Locate and identify every blood parasite.
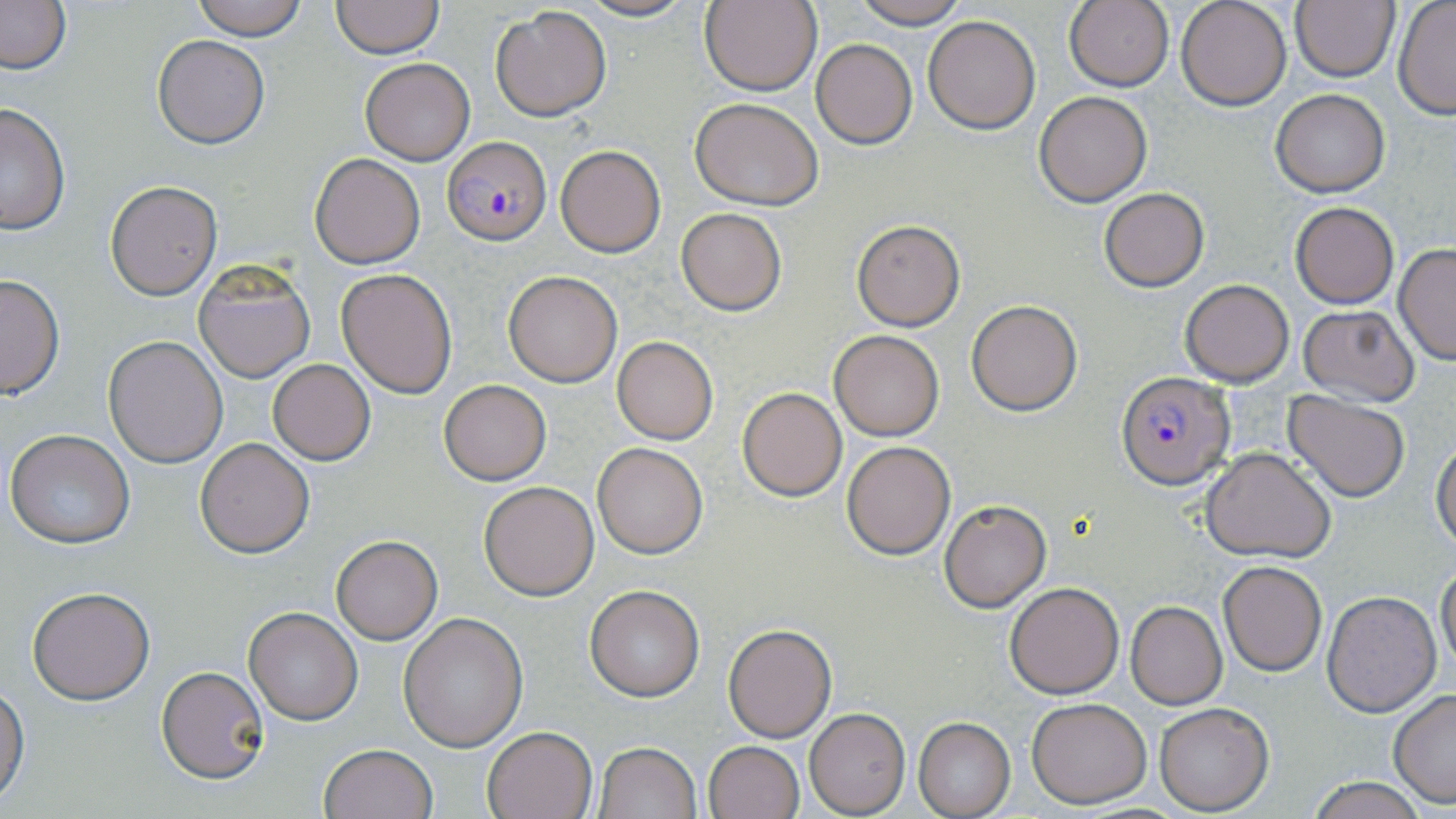
Approximate bounding boxes as (x1,y1)-(x2,y2) corner pairs in pixels.
Plasmodium falciparum-infected red blood cells: (443,135)-(551,245), (1115,371)-(1235,490).
No Plasmodium ovale, Plasmodium malariae, Plasmodium vivax, Babesia divergens, or Trypanosoma brucei observed.

Summary:
  - Uninfected red blood cell locations: (187,0)-(311,41), (575,0)-(696,21), (853,0)-(971,27), (1065,0)-(1176,92), (1176,0)-(1291,110), (1290,0)-(1398,83), (0,1)-(73,76), (330,1)-(444,59), (699,1)-(823,97), (1393,1)-(1456,120), (491,6)-(611,121), (922,16)-(1040,134), (152,34)-(271,149), (811,38)-(917,149), (359,58)-(474,165), (1270,90)-(1391,198), (1033,93)-(1152,207), (690,97)-(824,209), (0,103)-(71,234), (554,143)-(666,258), (311,153)-(424,268), (104,180)-(223,300), (1098,187)-(1210,292), (1289,202)-(1400,308), (677,208)-(786,315), (850,219)-(965,331), (1393,243)-(1456,365), (194,262)-(315,383), (335,267)-(457,398), (503,272)-(622,387), (0,273)-(65,398), (1179,279)-(1294,386), (967,301)-(1081,415), (1297,302)-(1420,405), (827,329)-(944,441), (103,335)-(229,468), (611,337)-(718,445), (268,359)-(376,466), (439,379)-(550,484), (738,387)-(848,501), (1285,393)-(1410,502), (5,429)-(135,549), (195,438)-(314,558), (1432,440)-(1456,553), (841,441)-(955,559), (592,442)-(709,558), (1201,447)-(1336,561), (479,481)-(600,600), (940,499)-(1051,611), (332,537)-(443,644), (1217,561)-(1327,676), (1436,563)-(1456,677), (1004,582)-(1124,699), (585,585)-(705,701), (28,586)-(155,704), (1321,590)-(1441,717), (1124,601)-(1227,709), (243,607)-(363,726), (398,613)-(528,751), (723,623)-(836,742), (157,666)-(269,783), (0,687)-(27,804), (1387,690)-(1456,809), (1025,697)-(1153,808), (1152,702)-(1274,815), (804,709)-(910,816), (914,717)-(1016,817), (481,724)-(598,819), (702,740)-(804,819), (594,742)-(702,818), (319,744)-(436,819), (1303,776)-(1432,819)
  - Slide-level diagnosis: Plasmodium falciparum
  - Stain: May-Grünwald-Giemsa
  - Magnification: 1000x
  - Image size: 1456×819 pixels
  - Field of view: one of a larger specimen
  - Preparation: thin blood film
  - Modality: optical microscopy